Assess this cell for malaria.
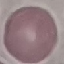

It is uninfected.

Acquired by smartphone through the microscope eyepiece. Giemsa-stained preparation. Thin smear of blood. Cell patch, automatically extracted from a larger field of view and resized to 64 × 64 pixels.